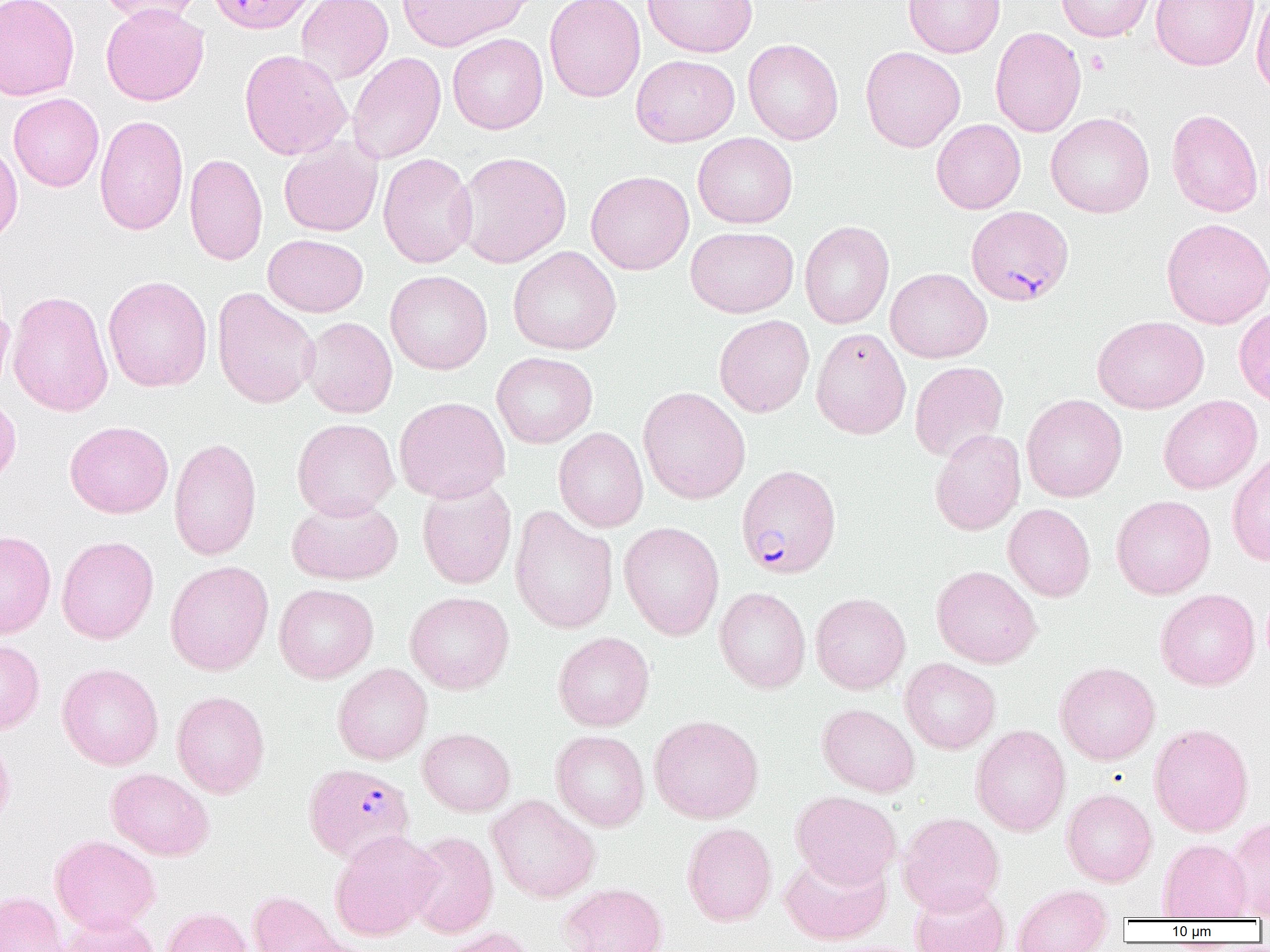

Approximate bounding boxes as named x1/y1/x2/y2 corners in pixels. Platelet locations: (x1=1085, y1=50, x2=1109, y2=76). Plasmodium falciparum-infected red blood cell locations: (x1=206, y1=0, x2=317, y2=34), (x1=966, y1=205, x2=1074, y2=307), (x1=736, y1=464, x2=842, y2=579), (x1=303, y1=763, x2=415, y2=864). Uninfected red blood cell locations: (x1=0, y1=0, x2=80, y2=101), (x1=96, y1=0, x2=204, y2=25), (x1=296, y1=0, x2=393, y2=84), (x1=544, y1=0, x2=645, y2=102), (x1=643, y1=0, x2=758, y2=58), (x1=903, y1=0, x2=1005, y2=58), (x1=1056, y1=0, x2=1157, y2=42), (x1=1151, y1=0, x2=1258, y2=70), (x1=1251, y1=0, x2=1270, y2=98), (x1=397, y1=1, x2=533, y2=52), (x1=100, y1=3, x2=209, y2=106), (x1=990, y1=26, x2=1086, y2=137), (x1=448, y1=33, x2=548, y2=134), (x1=743, y1=39, x2=844, y2=145), (x1=860, y1=46, x2=965, y2=152), (x1=239, y1=49, x2=352, y2=160), (x1=347, y1=52, x2=446, y2=164), (x1=631, y1=55, x2=739, y2=147), (x1=8, y1=93, x2=104, y2=192), (x1=1166, y1=109, x2=1263, y2=217), (x1=1045, y1=112, x2=1155, y2=218), (x1=94, y1=115, x2=189, y2=236), (x1=931, y1=119, x2=1026, y2=214), (x1=692, y1=132, x2=797, y2=228), (x1=279, y1=137, x2=382, y2=237), (x1=0, y1=139, x2=23, y2=246), (x1=454, y1=152, x2=572, y2=268), (x1=184, y1=153, x2=268, y2=266), (x1=377, y1=153, x2=478, y2=268), (x1=585, y1=171, x2=694, y2=275), (x1=1161, y1=217, x2=1270, y2=328), (x1=799, y1=221, x2=895, y2=329), (x1=685, y1=227, x2=798, y2=318), (x1=263, y1=234, x2=368, y2=316), (x1=508, y1=246, x2=621, y2=355), (x1=885, y1=268, x2=992, y2=363), (x1=385, y1=270, x2=493, y2=375), (x1=103, y1=276, x2=212, y2=392), (x1=0, y1=288, x2=15, y2=399), (x1=212, y1=288, x2=319, y2=409), (x1=7, y1=290, x2=114, y2=417), (x1=1233, y1=307, x2=1270, y2=407), (x1=714, y1=314, x2=814, y2=417), (x1=301, y1=316, x2=398, y2=418), (x1=1092, y1=316, x2=1209, y2=414), (x1=811, y1=327, x2=911, y2=439), (x1=491, y1=352, x2=598, y2=448), (x1=909, y1=361, x2=1009, y2=462), (x1=638, y1=386, x2=751, y2=504), (x1=0, y1=393, x2=21, y2=491), (x1=1021, y1=394, x2=1127, y2=502), (x1=1158, y1=395, x2=1262, y2=494), (x1=393, y1=396, x2=510, y2=504), (x1=292, y1=418, x2=399, y2=520), (x1=65, y1=421, x2=174, y2=518), (x1=553, y1=427, x2=648, y2=532), (x1=930, y1=428, x2=1025, y2=536), (x1=169, y1=437, x2=262, y2=560), (x1=1226, y1=450, x2=1270, y2=566), (x1=416, y1=479, x2=517, y2=590), (x1=1111, y1=495, x2=1216, y2=599), (x1=287, y1=496, x2=403, y2=585), (x1=1003, y1=504, x2=1095, y2=601), (x1=509, y1=505, x2=618, y2=634), (x1=618, y1=521, x2=725, y2=641), (x1=0, y1=530, x2=56, y2=638), (x1=56, y1=535, x2=158, y2=644), (x1=165, y1=560, x2=274, y2=675), (x1=931, y1=565, x2=1042, y2=668), (x1=274, y1=583, x2=378, y2=683), (x1=714, y1=587, x2=811, y2=693), (x1=1155, y1=588, x2=1260, y2=691), (x1=405, y1=591, x2=514, y2=694), (x1=810, y1=592, x2=911, y2=694), (x1=553, y1=631, x2=655, y2=731), (x1=0, y1=638, x2=45, y2=734), (x1=900, y1=658, x2=1001, y2=754), (x1=57, y1=662, x2=164, y2=770), (x1=1054, y1=662, x2=1160, y2=765), (x1=332, y1=663, x2=432, y2=765), (x1=171, y1=691, x2=270, y2=798), (x1=817, y1=704, x2=920, y2=796), (x1=649, y1=715, x2=763, y2=823), (x1=1148, y1=722, x2=1254, y2=837), (x1=971, y1=724, x2=1071, y2=836), (x1=418, y1=728, x2=516, y2=816), (x1=0, y1=730, x2=16, y2=831), (x1=551, y1=730, x2=650, y2=831), (x1=106, y1=768, x2=214, y2=861), (x1=1061, y1=789, x2=1157, y2=887), (x1=791, y1=791, x2=902, y2=888), (x1=487, y1=795, x2=600, y2=903), (x1=897, y1=812, x2=1005, y2=916), (x1=1225, y1=816, x2=1270, y2=919), (x1=682, y1=822, x2=777, y2=926), (x1=329, y1=830, x2=440, y2=941), (x1=404, y1=830, x2=499, y2=938), (x1=50, y1=834, x2=160, y2=934), (x1=1158, y1=839, x2=1252, y2=920), (x1=780, y1=849, x2=892, y2=945), (x1=559, y1=882, x2=668, y2=952), (x1=909, y1=883, x2=1010, y2=952), (x1=1012, y1=884, x2=1113, y2=952), (x1=247, y1=890, x2=344, y2=952), (x1=0, y1=891, x2=66, y2=952), (x1=160, y1=907, x2=253, y2=952), (x1=54, y1=912, x2=160, y2=952), (x1=438, y1=926, x2=539, y2=952), (x1=282, y1=934, x2=376, y2=952). Slide-level diagnosis: Plasmodium falciparum. Thin blood smear. One field of a larger specimen. Optical microscopy. Image is 1270×952 pixels. Captured at 1000x magnification.